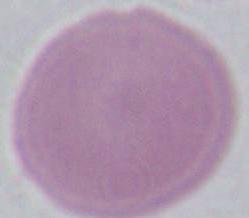

Photomicrograph. 1000x magnification. An erythrocyte is shown.